Name the blood parasite species.
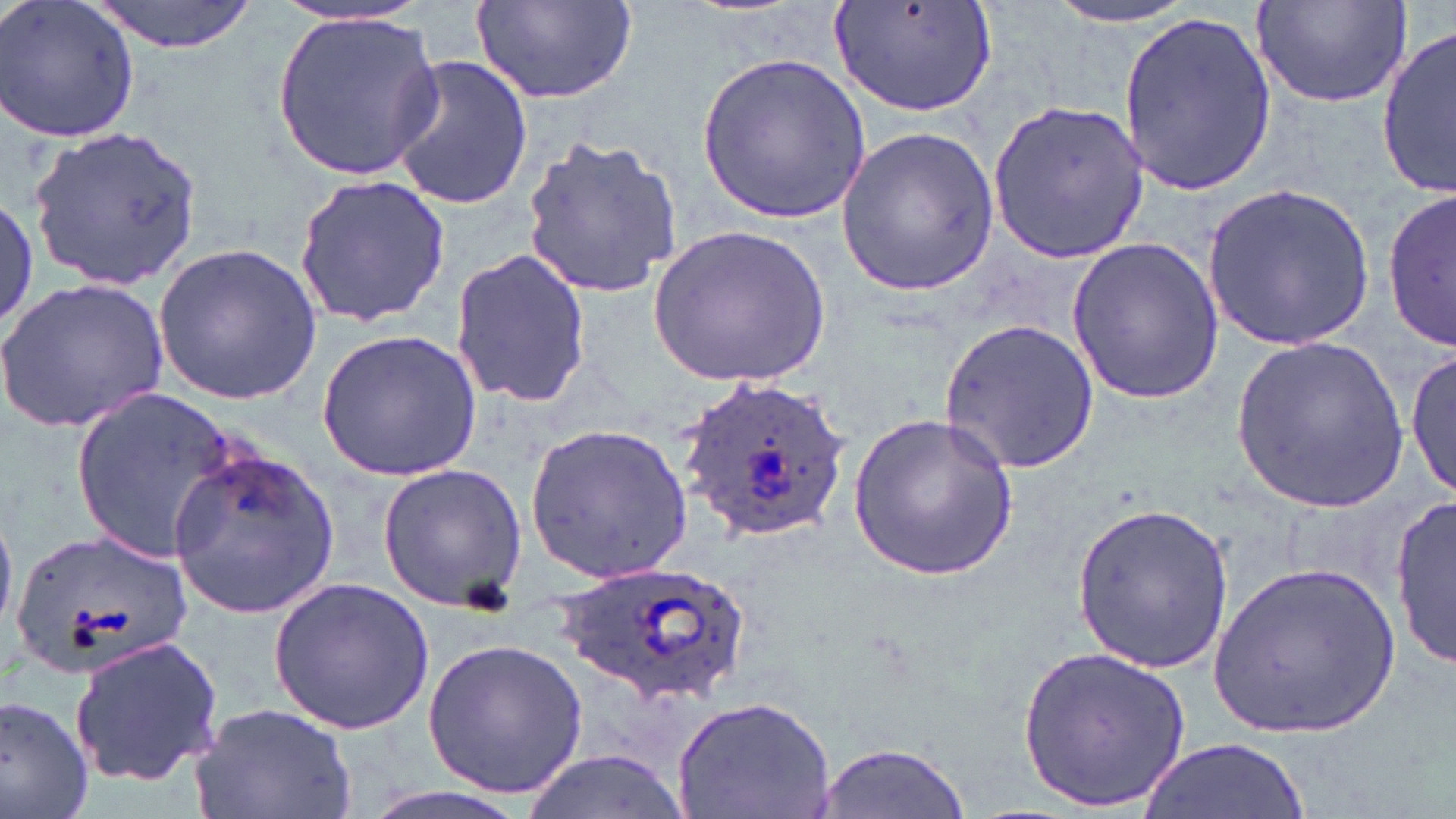

Plasmodium ovale.

Summary:
  - Coordinate format: approximate bounding boxes as [x1, y1, x2, y2] in pixels
  - Uninfected red blood cell locations: [88, 0, 259, 55], [471, 0, 639, 107], [827, 0, 998, 116], [1, 1, 138, 144], [1251, 2, 1413, 110], [1042, 3, 1204, 28], [269, 9, 444, 179], [1118, 10, 1277, 196], [1378, 21, 1455, 200], [699, 51, 872, 227], [388, 54, 533, 211], [987, 99, 1148, 263], [30, 125, 206, 290], [834, 128, 1000, 296], [522, 134, 685, 300], [294, 175, 450, 328], [1202, 180, 1374, 350], [1382, 189, 1456, 355], [0, 192, 39, 329], [650, 223, 830, 386], [1065, 239, 1223, 407], [153, 242, 323, 407], [448, 247, 593, 410], [0, 272, 172, 435], [940, 316, 1099, 474], [316, 328, 484, 481], [1231, 336, 1412, 517], [1408, 345, 1455, 501], [71, 385, 241, 560], [849, 408, 1021, 585], [527, 422, 696, 586], [167, 443, 341, 621], [377, 463, 528, 611], [1392, 497, 1454, 669], [1067, 502, 1239, 673], [10, 525, 192, 683], [1208, 560, 1399, 741], [265, 576, 437, 736], [67, 632, 223, 787], [421, 636, 588, 799], [1018, 642, 1194, 812], [0, 692, 95, 819], [672, 694, 837, 819], [192, 699, 359, 819], [1137, 737, 1312, 819], [810, 740, 975, 818], [517, 747, 690, 819]
  - Plasmodium ovale-infected red blood cell locations: [677, 376, 850, 545], [562, 565, 743, 704]
  - Preparation: thin blood smear
  - Modality: optical microscopy
  - Image size: 1456×819 pixels
  - Field of view: single
  - Magnification: 1000x
  - Stain: May-Grünwald-Giemsa